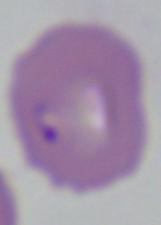
identification = Babesia
modality = micrograph
magnification = 1000x